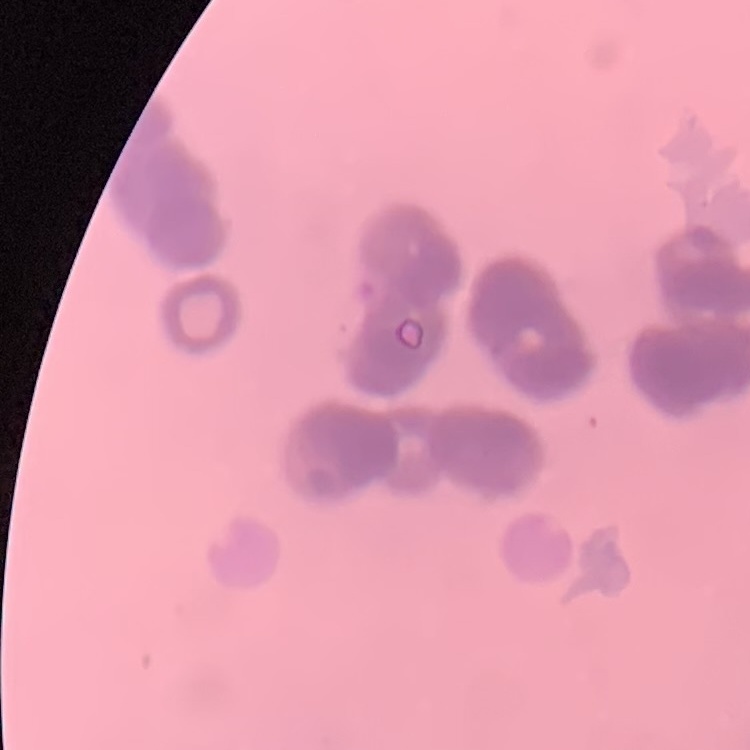
Summary:
  - Red blood cell morphology: rouleaux formation
  - Image type: square crop of a larger photomicrograph
  - Stain: Field's or Giemsa
  - Preparation: thin blood smear